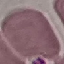

Malaria status: uninfected. Acquired by smartphone through the microscope eyepiece. Thin smear of blood. Giemsa stain. Cell patch, automatically extracted from a larger field of view and resized to 64 × 64 pixels.